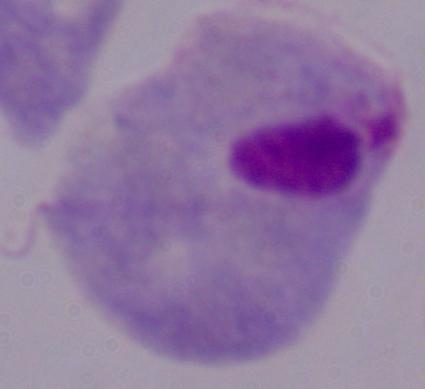 Photomicrograph. A trichomonad is shown. Captured at 1000x magnification.